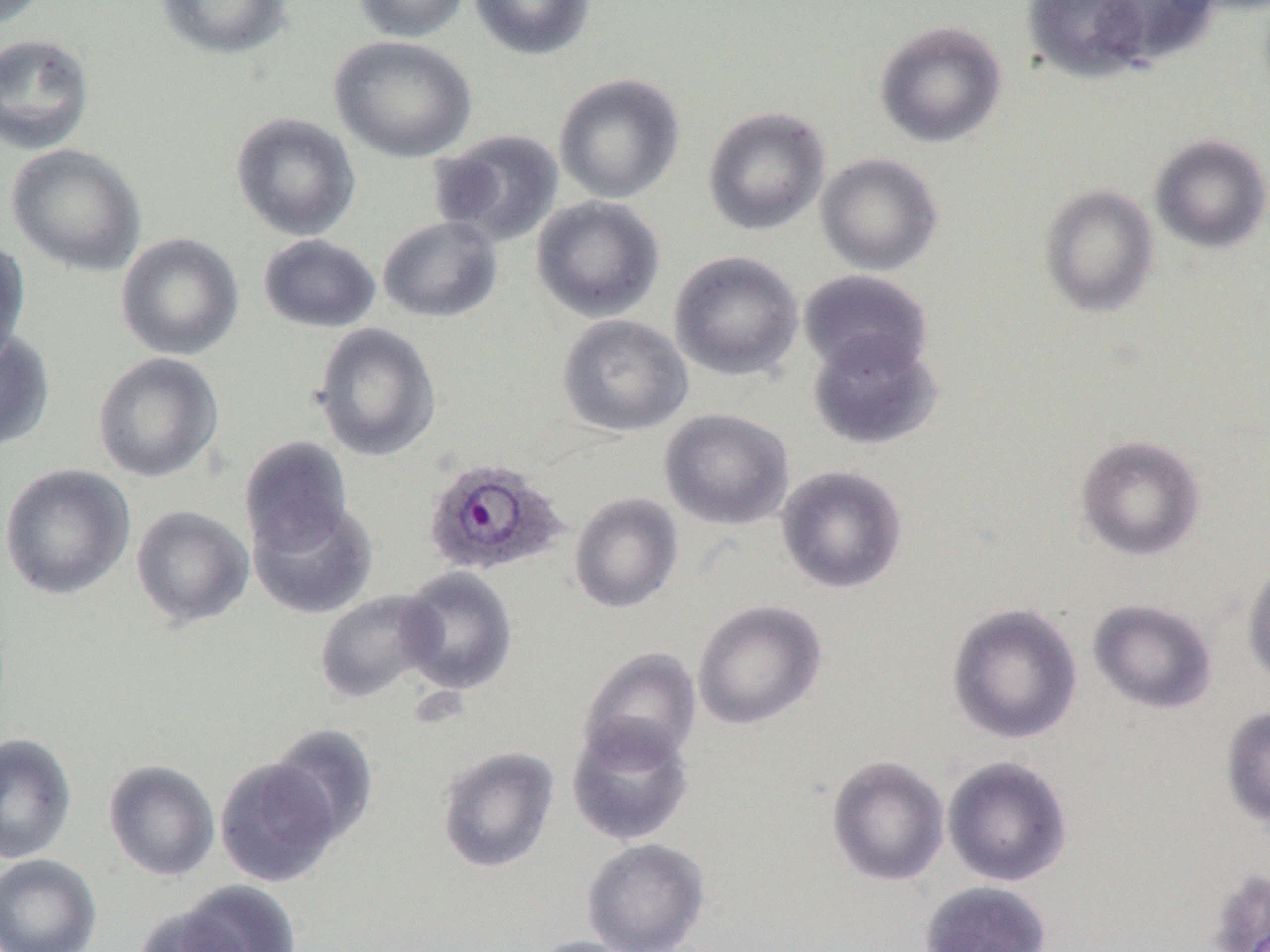

{
  "slide_level_diagnosis": "Plasmodium ovale",
  "modality": "optical microscopy",
  "plasmodium_ovale_infected_red_blood_cell_locations": "approximate bounding boxes as named x1/y1/x2/y2 corners in pixels: (x1=421, y1=456, x2=569, y2=577)",
  "field_of_view": "one of a larger specimen",
  "magnification": "1000x",
  "uninfected_red_blood_cell_locations": "approximate bounding boxes as named x1/y1/x2/y2 corners in pixels: (x1=0, y1=0, x2=49, y2=29), (x1=153, y1=0, x2=294, y2=61), (x1=353, y1=0, x2=471, y2=43), (x1=469, y1=0, x2=596, y2=60), (x1=1023, y1=0, x2=1151, y2=82), (x1=1095, y1=0, x2=1221, y2=68), (x1=874, y1=19, x2=1008, y2=148), (x1=0, y1=32, x2=95, y2=155), (x1=330, y1=35, x2=477, y2=162), (x1=554, y1=73, x2=685, y2=204), (x1=702, y1=106, x2=830, y2=236), (x1=230, y1=111, x2=361, y2=242), (x1=429, y1=128, x2=565, y2=247), (x1=1150, y1=134, x2=1270, y2=253), (x1=5, y1=143, x2=147, y2=276), (x1=815, y1=153, x2=943, y2=276), (x1=1039, y1=185, x2=1159, y2=317), (x1=531, y1=195, x2=665, y2=322), (x1=378, y1=215, x2=503, y2=323), (x1=115, y1=232, x2=244, y2=360), (x1=258, y1=233, x2=381, y2=333), (x1=0, y1=241, x2=31, y2=365), (x1=669, y1=250, x2=804, y2=382), (x1=798, y1=270, x2=933, y2=381), (x1=557, y1=314, x2=693, y2=437), (x1=312, y1=322, x2=441, y2=461), (x1=0, y1=330, x2=55, y2=452), (x1=807, y1=331, x2=942, y2=451), (x1=92, y1=352, x2=224, y2=483), (x1=659, y1=408, x2=794, y2=530), (x1=1076, y1=434, x2=1205, y2=561), (x1=239, y1=436, x2=355, y2=555), (x1=0, y1=462, x2=135, y2=601), (x1=776, y1=464, x2=908, y2=594), (x1=568, y1=491, x2=684, y2=614), (x1=247, y1=498, x2=378, y2=619), (x1=130, y1=505, x2=254, y2=629), (x1=1242, y1=560, x2=1270, y2=689), (x1=397, y1=566, x2=519, y2=696), (x1=314, y1=589, x2=443, y2=703), (x1=1087, y1=598, x2=1218, y2=715), (x1=692, y1=599, x2=826, y2=730), (x1=946, y1=602, x2=1082, y2=745), (x1=579, y1=647, x2=702, y2=767), (x1=1220, y1=706, x2=1270, y2=828), (x1=566, y1=716, x2=695, y2=846), (x1=267, y1=722, x2=380, y2=845), (x1=0, y1=733, x2=77, y2=864), (x1=436, y1=745, x2=560, y2=873), (x1=825, y1=755, x2=950, y2=886), (x1=942, y1=755, x2=1073, y2=887), (x1=214, y1=757, x2=342, y2=887), (x1=102, y1=759, x2=220, y2=882), (x1=581, y1=837, x2=710, y2=952), (x1=0, y1=854, x2=101, y2=952), (x1=1207, y1=868, x2=1270, y2=952), (x1=919, y1=880, x2=1052, y2=952), (x1=164, y1=881, x2=303, y2=952), (x1=131, y1=902, x2=259, y2=952), (x1=527, y1=935, x2=645, y2=952)",
  "preparation": "thin blood smear",
  "image_size": "1270×952 pixels"
}